Describe the morphology of the erythrocytes.
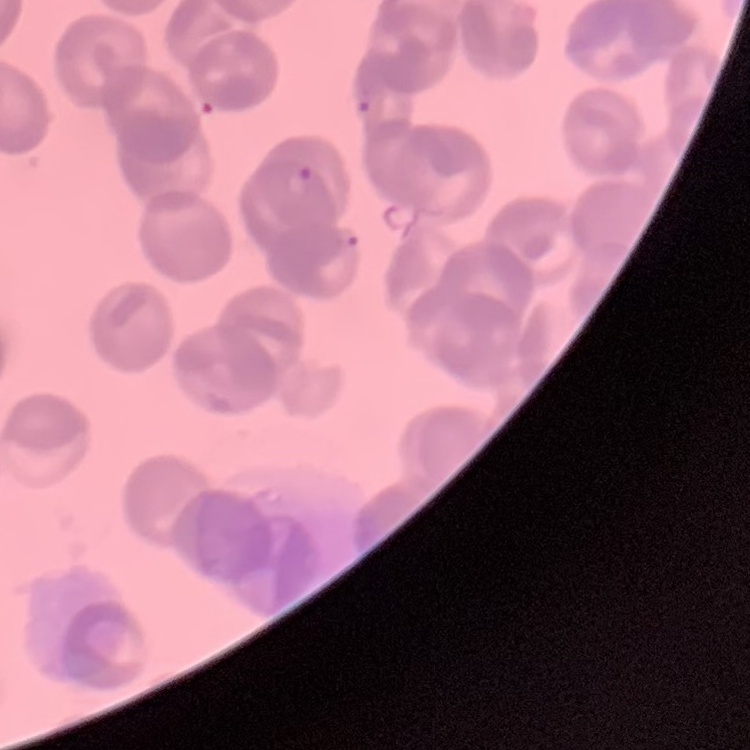
They show rouleaux formation.

Field's or Giemsa stain. One tile cut from a larger photomicrograph. Thin peripheral smear.